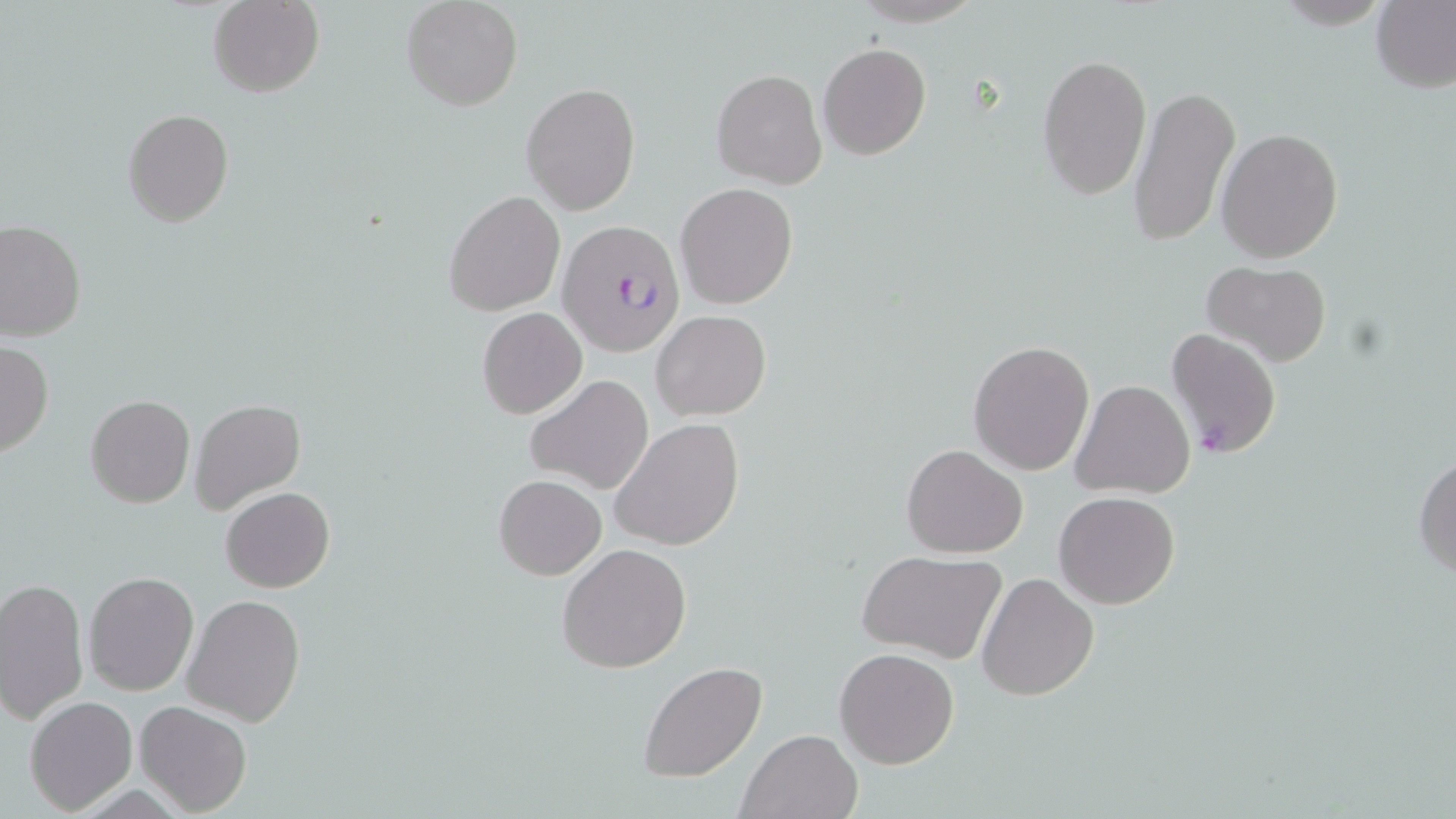
{
  "plasmodium_falciparum_infected_red_blood_cell_locations": "approximate bounding boxes as (x1,y1)-(x2,y2) corner pairs in pixels: (558,221)-(688,356), (1166,328)-(1282,458)",
  "slide_level_diagnosis": "Plasmodium falciparum",
  "magnification": "1000x",
  "modality": "optical microscopy",
  "preparation": "thin blood film",
  "image_size": "1456×819 pixels",
  "stain": "May-Grünwald-Giemsa",
  "field_of_view": "single",
  "uninfected_red_blood_cell_locations": "approximate bounding boxes as (x1,y1)-(x2,y2) corner pairs in pixels: (401,0)-(523,111), (1372,0)-(1456,92), (208,1)-(324,98), (818,42)-(931,160), (1038,53)-(1150,199), (712,68)-(828,189), (520,81)-(640,216), (1127,81)-(1240,251), (122,109)-(233,228), (1216,128)-(1344,263), (675,182)-(798,309), (444,190)-(564,317), (0,218)-(86,341), (1199,260)-(1331,366), (476,307)-(587,420), (651,310)-(771,421), (968,339)-(1095,474), (0,340)-(53,458), (525,373)-(654,495), (1071,379)-(1196,498), (86,395)-(195,508), (190,399)-(304,511), (610,418)-(744,551), (903,444)-(1028,559), (1413,452)-(1456,580), (494,474)-(606,581), (221,487)-(334,592), (1053,491)-(1180,608), (557,543)-(692,671), (858,550)-(1008,663), (84,570)-(198,695), (977,572)-(1099,701), (0,578)-(89,727), (182,592)-(306,727), (835,645)-(960,768), (639,662)-(767,782), (24,696)-(136,814), (134,701)-(254,816), (735,728)-(862,819)"
}